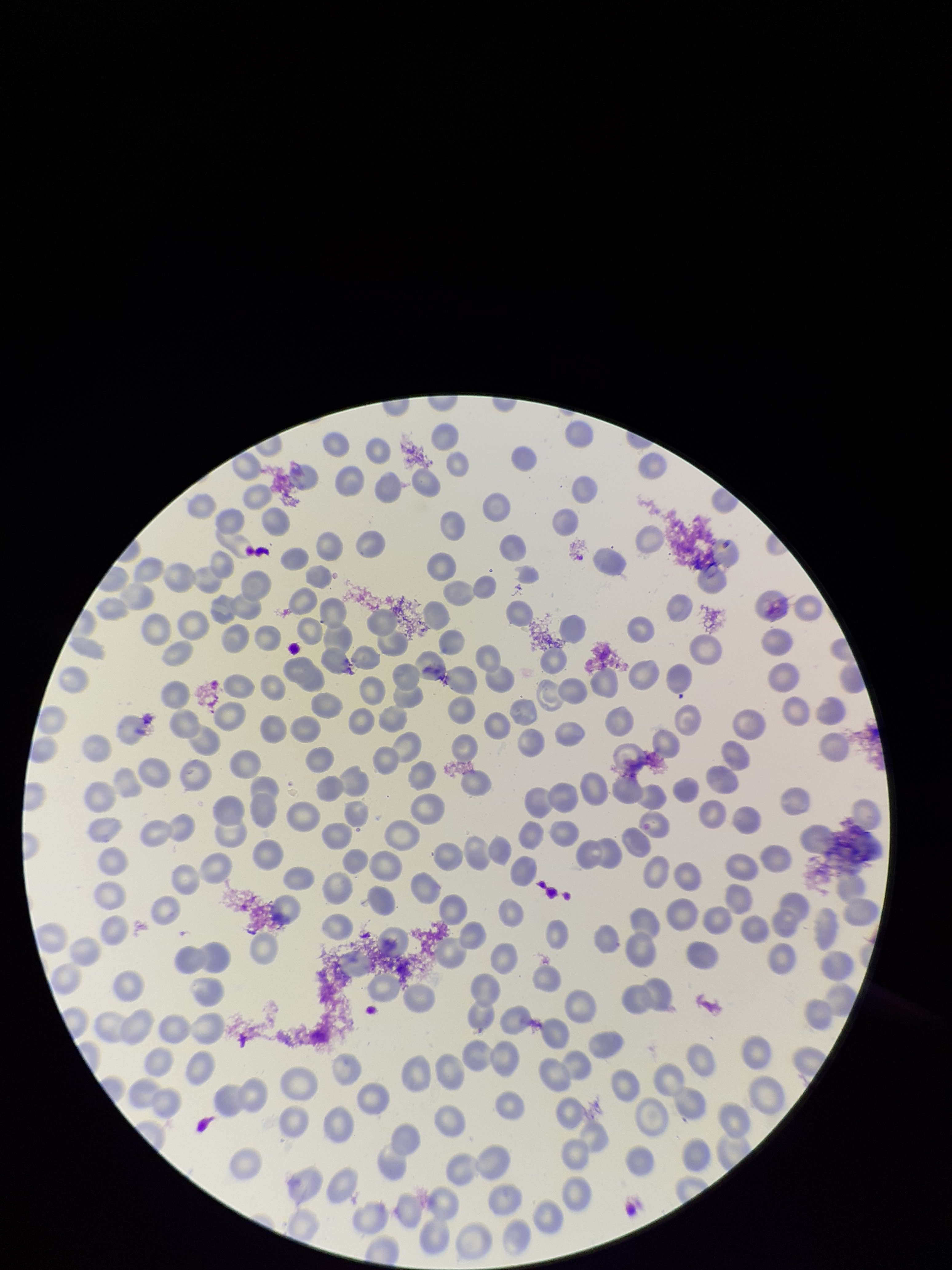
red blood cell count = 247
capture = smartphone photograph through the microscope eyepiece
parasitized red blood cell count = 0
stain = Giemsa
patient malaria status = negative
image size = 952×1270 pixels
parasitized red blood cells = none identified
preparation = thin smear
field of view = single